Locate every Plasmodium parasite.
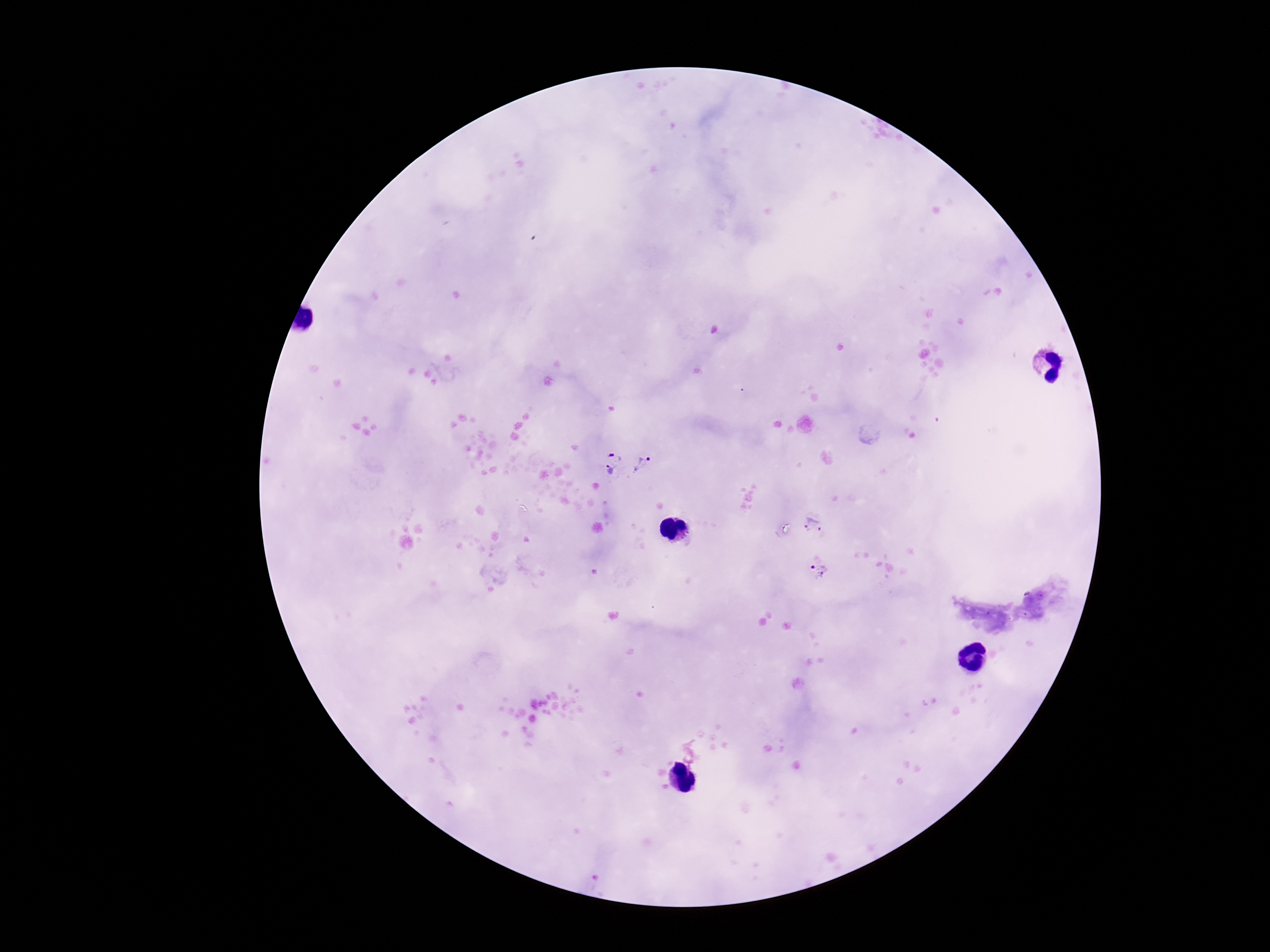

Approximate centers as (x, y) in pixels.
Plasmodium parasites: (615, 450), (643, 463), (608, 472), (812, 523), (819, 570).

Patient malaria status: infected. Image is 1270×952 pixels. 100x magnification. Single field of view. Giemsa stain. Thick blood smear. Smartphone photograph taken through the microscope eyepiece.